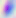

{
  "magnification": "400x",
  "identification": "Toxoplasma gondii",
  "modality": "micrograph"
}